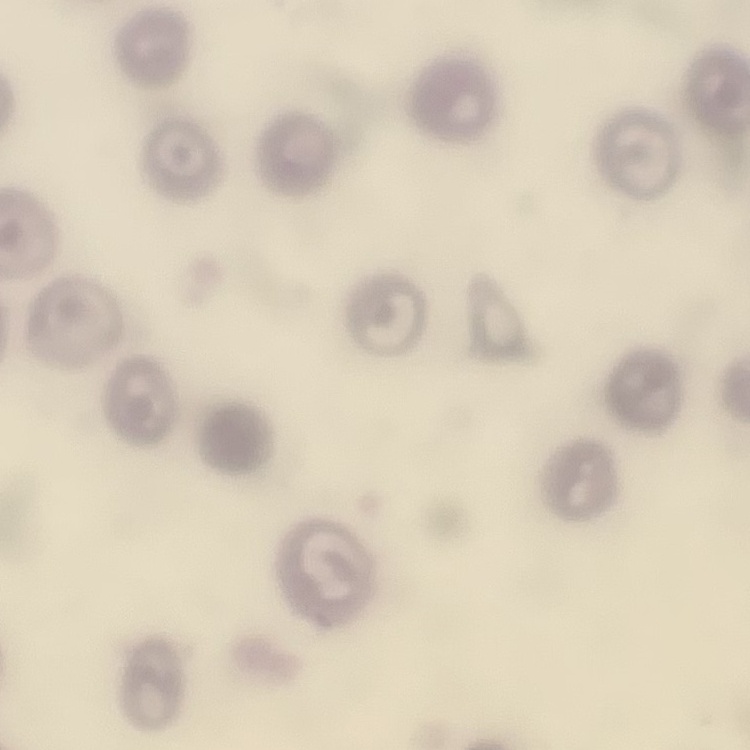 The red blood cells show no rouleaux formation. Thin blood film. Square crop of a larger photomicrograph. Field's or Giemsa stain.